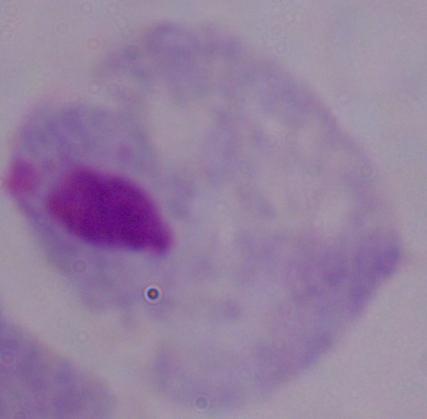

{
  "modality": "micrograph",
  "magnification": "1000x",
  "identification": "trichomonad"
}